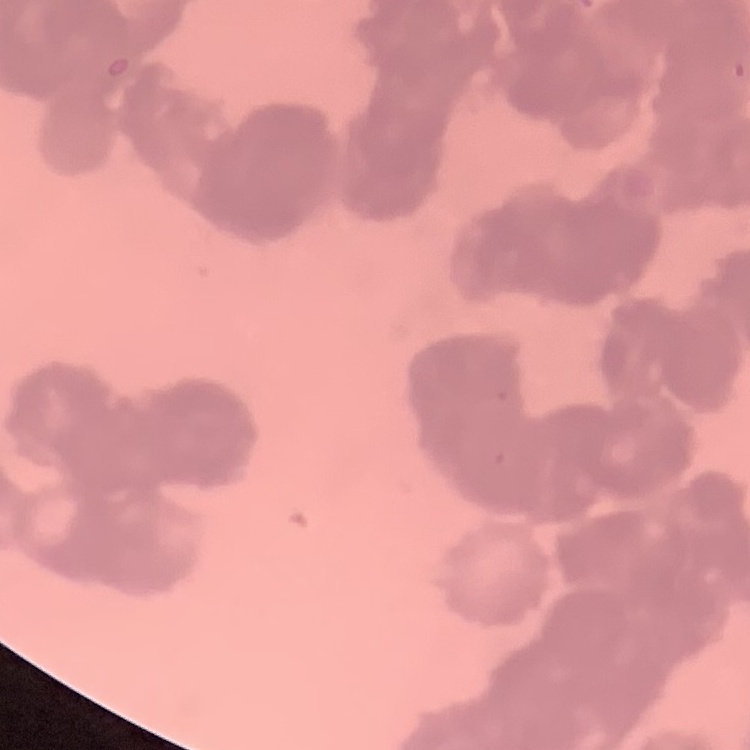
red blood cell morphology = rouleaux formation
preparation = thin peripheral smear
stain = Field's or Giemsa
image type = one tile cut from a larger photomicrograph